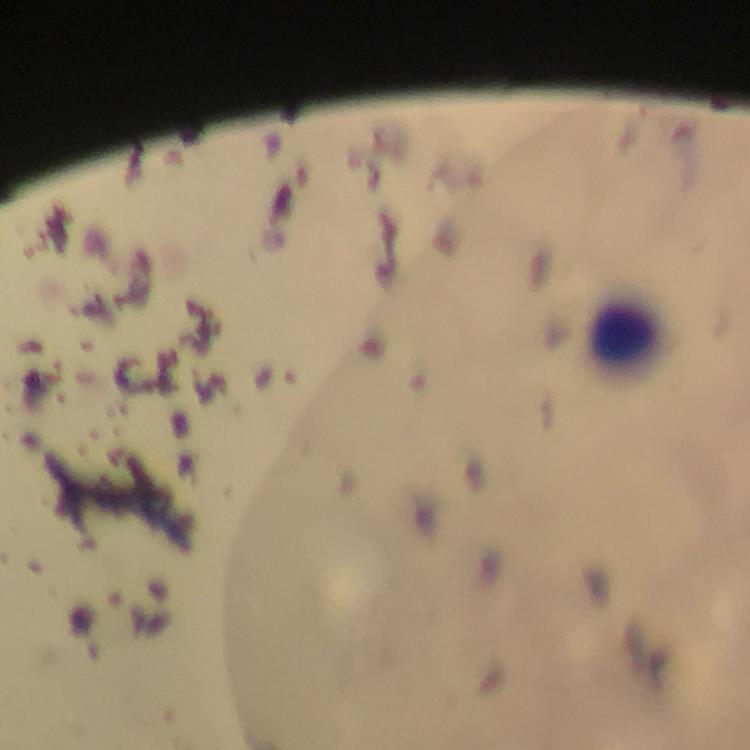
Approximate centers as [x, y] in pixels.
Summary:
  - Leukocyte locations: [629, 343]
  - Plasmodium parasite locations: [274, 244]
  - Immersion oil: applied
  - Capture: smartphone mounted on the microscope
  - Magnification: 100x
  - Stain: Giemsa
  - Cropped from: a single field of view
  - Preparation: thick blood smear
  - Image size: 750×750 pixels
  - Context: from a diagnostic examination for malaria